Identify the parasite.
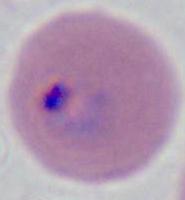
Plasmodium.

Summary:
  - Magnification: 400x or 1000x
  - Modality: photomicrograph